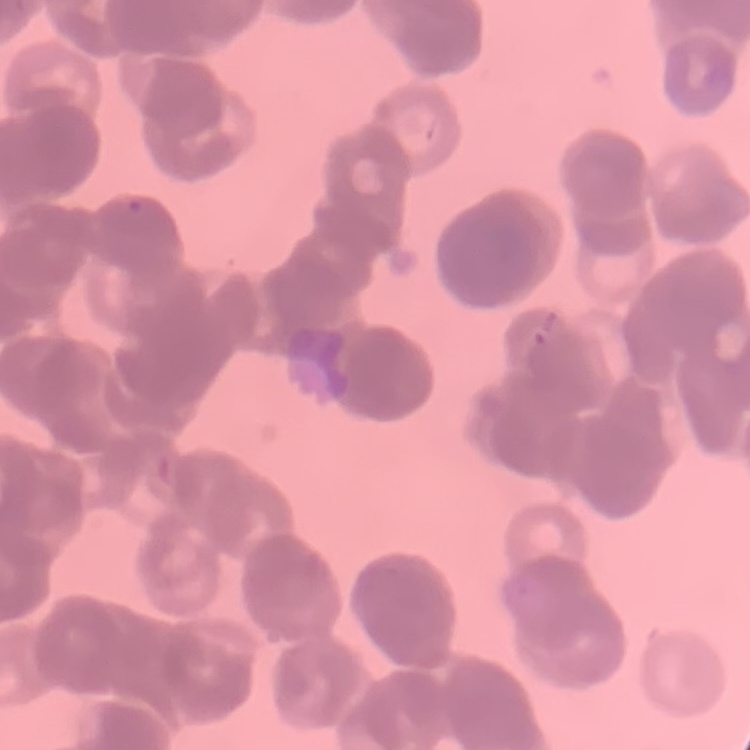
Summary:
  - Erythrocyte morphology: rouleaux formation
  - Image type: square crop of a larger photomicrograph
  - Stain: Field's or Giemsa
  - Preparation: thin blood smear